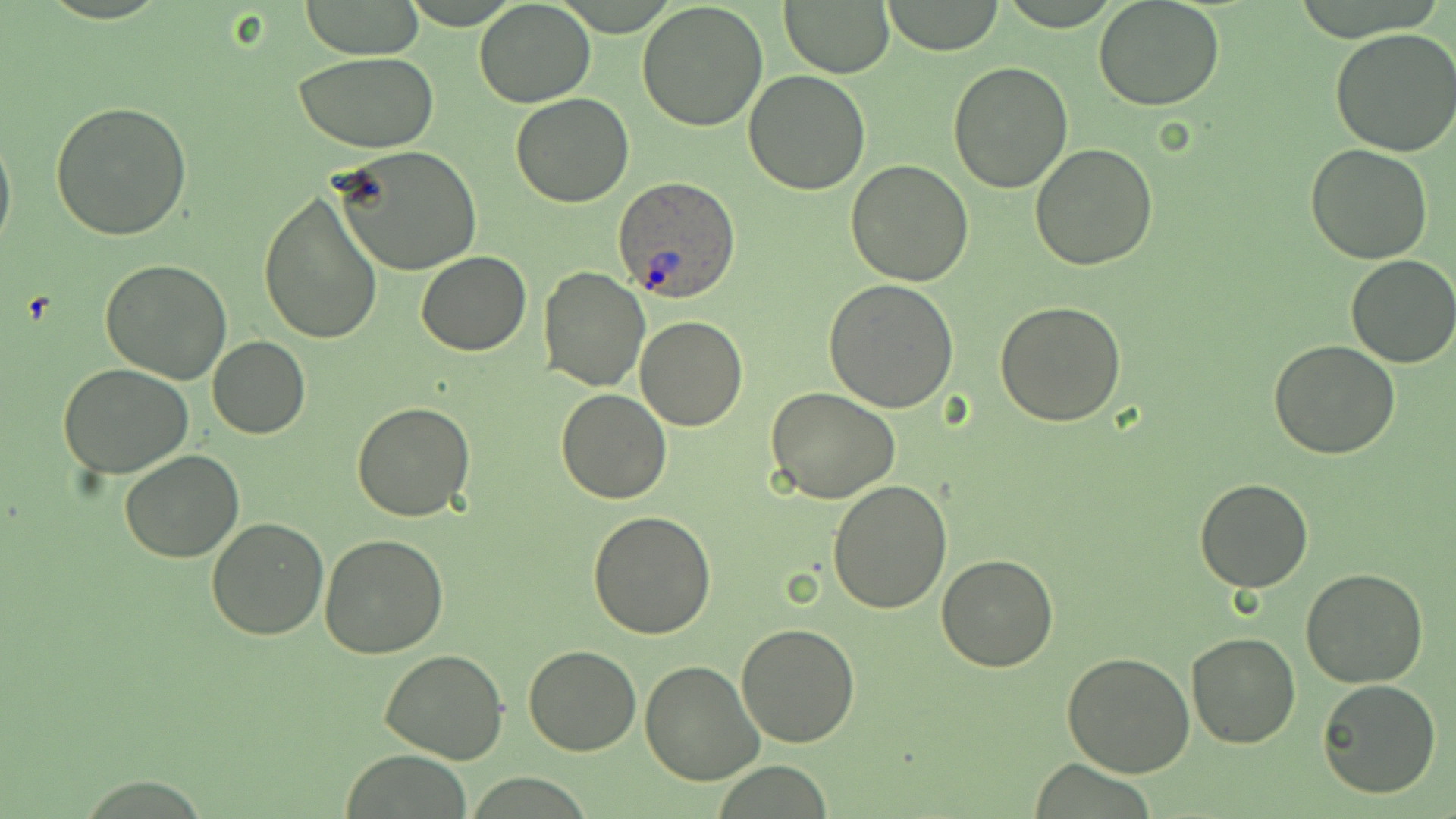

Summary:
  - Coordinate format: approximate bounding boxes as (x1, y1, x2, y2) in pixels
  - Uninfected red blood cell locations: (778, 0, 896, 77), (1094, 0, 1225, 112), (299, 1, 424, 60), (474, 1, 597, 108), (880, 1, 1004, 54), (638, 2, 769, 134), (1330, 27, 1456, 157), (293, 51, 438, 152), (947, 62, 1074, 193), (743, 70, 870, 193), (511, 92, 635, 208), (50, 100, 192, 239), (0, 121, 15, 260), (1029, 143, 1159, 270), (1305, 143, 1435, 263), (328, 144, 482, 276), (844, 160, 975, 285), (258, 191, 385, 345), (415, 251, 532, 355), (1345, 254, 1456, 370), (100, 258, 232, 384), (539, 266, 648, 391), (825, 278, 959, 411), (995, 301, 1127, 427), (634, 315, 749, 430), (207, 336, 310, 439), (1269, 339, 1400, 458), (60, 364, 193, 478), (766, 386, 900, 505), (555, 388, 672, 505), (352, 400, 476, 521), (118, 450, 244, 562), (1195, 478, 1314, 594), (826, 480, 952, 614), (586, 511, 717, 641), (206, 518, 329, 640), (320, 532, 450, 660), (936, 555, 1060, 672), (1302, 568, 1426, 687), (734, 623, 861, 748), (1186, 632, 1300, 748), (524, 643, 638, 754), (381, 649, 511, 765), (1060, 651, 1195, 777), (640, 661, 763, 785), (1316, 679, 1442, 800), (341, 751, 471, 819)
  - Plasmodium ovale-infected red blood cell locations: (614, 176, 741, 301)
  - Slide-level diagnosis: Plasmodium ovale
  - Stain: May-Grünwald-Giemsa
  - Field of view: single
  - Modality: light microscopy
  - Magnification: 1000x
  - Preparation: thin blood smear
  - Image size: 1456×819 pixels